Identify the parasite.
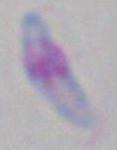
This is Toxoplasma gondii.

magnification = 1000x
modality = micrograph